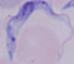

Summary:
  - Identification: trypanosome
  - Modality: micrograph
  - Magnification: 1000x